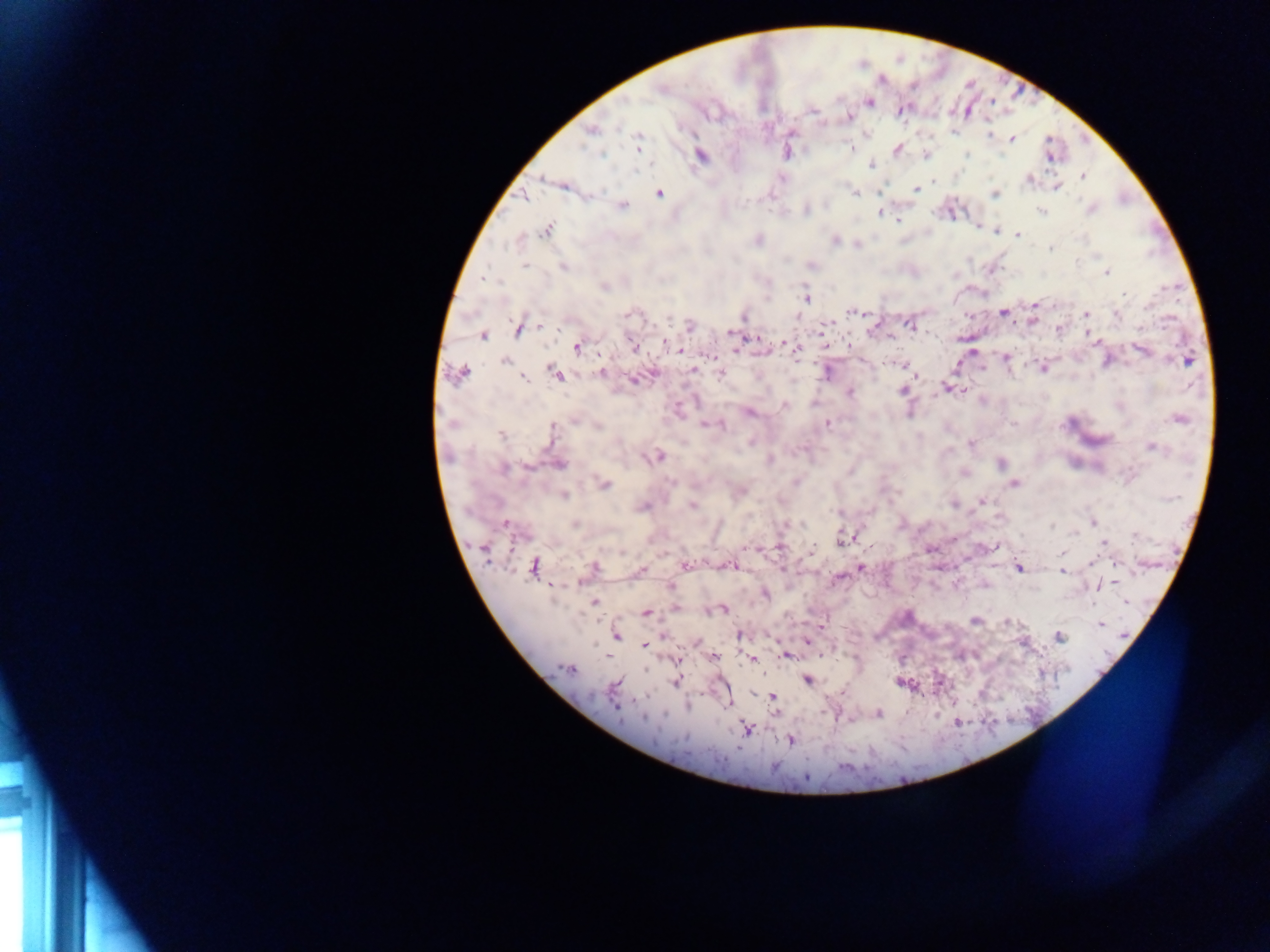

Approximate centers as x y in pixels. Malaria parasite locations: 660 88; 870 102; 902 110; 813 111; 849 117; 591 130; 988 134; 1013 140; 638 141; 851 147; 898 150; 601 154; 968 154; 701 156; 926 156; 1050 159; 870 165; 1082 176; 544 178; 781 178; 1029 179; 934 182; 1057 188; 916 189; 879 192; 659 193; 855 193; 995 194; 524 197; 623 206; 1091 209; 806 211; 1041 211; 879 213; 899 220; 979 228; 546 229; 995 231; 1018 235; 759 239; 835 240; 518 241; 858 246; 1050 248; 1077 261; 525 266; 812 266; 563 268; 1107 272; 485 279; 604 287; 1124 294; 806 298; 1035 304; 851 311; 1003 313; 628 314; 1086 314; 1117 314; 744 317; 1033 320; 909 324; 540 326; 690 326; 517 330; 730 333; 482 336; 1095 340; 665 342; 788 344; 849 346; 577 347; 633 347; 796 348; 735 349; 678 350; 1143 350; 972 351; 1006 357; 1188 361; 505 362; 904 365; 982 368; 1044 368; 693 370; 461 373; 601 373; 827 373; 556 374; 721 374; 523 378; 631 380; 946 388; 901 391; 963 391; 850 392; 784 405; 749 413; 1178 419; 574 420; 827 423; 1013 423; 706 425; 598 426; 721 426; 553 432; 501 435; 750 442; 971 444; 1151 447; 658 457; 770 460; 1001 463; 560 464; 527 467; 503 469; 671 482; 796 482; 1015 483; 605 484; 741 491; 565 495; 982 500; 954 505; 692 506; 642 507; 838 513; 803 523; 1093 523; 505 524; 574 524; 1052 525; 1075 533; 1136 535; 842 538; 1104 543; 994 546; 779 547; 748 548; 931 549; 812 550; 622 553; 1061 554; 1092 561; 686 565; 534 566; 730 566; 595 567; 860 567; 1019 568; 641 569; 1063 572; 578 583; 671 586; 1099 586; 766 594; 594 602; 724 610; 646 613; 975 620; 1007 622; 1100 624; 740 635; 617 636; 1059 636; 807 642; 644 645; 785 655; 606 656; 714 657; 679 660; 752 660; 569 668; 676 681; 807 681; 616 685; 773 697; 616 706; 878 714; 644 718; 747 729; 791 740; 806 778. Photographed through a microscope with a mobile-phone camera. Thick blood film. Image is 1270×952 pixels. Sample from Ghana. One field of view.